Assess this cell for malaria.
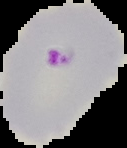
It is parasitized.

Segmented cell region on a black background. Image is 127×148 pixels. From a thin blood smear.